Report the malaria status of this cell.
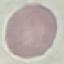
Uninfected.

Summary:
  - Preparation: thin smear
  - Capture: smartphone through the microscope eyepiece
  - Stain: Giemsa
  - Image type: cell patch, automatically extracted from a larger field of view and resized to 64 × 64 pixels